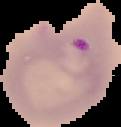

Summary:
  - Preparation: thin blood film
  - Image size: 121×127 pixels
  - Image type: cell region segmented out of the field of view; surrounding area masked to black
  - Malaria status: parasitized